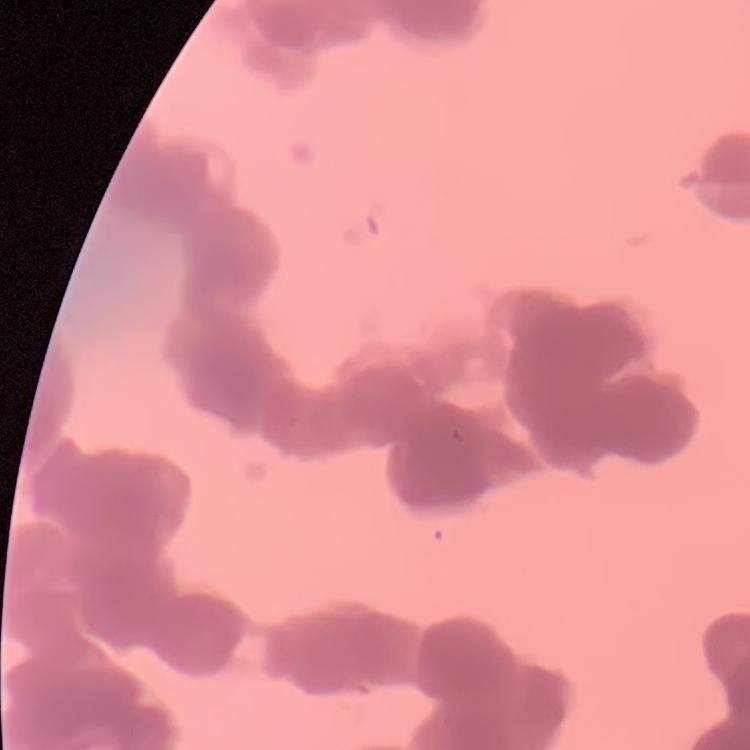
Summary:
  - Erythrocyte morphology: rouleaux formation
  - Preparation: thin blood film
  - Image type: one tile cut from a larger photomicrograph
  - Stain: Field's or Giemsa